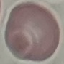

Summary:
  - Malaria status: uninfected
  - Stain: Giemsa
  - Image type: cell patch, automatically extracted from a larger field of view and resized to 64 × 64 pixels
  - Capture: smartphone camera at the microscope eyepiece
  - Preparation: thin blood smear